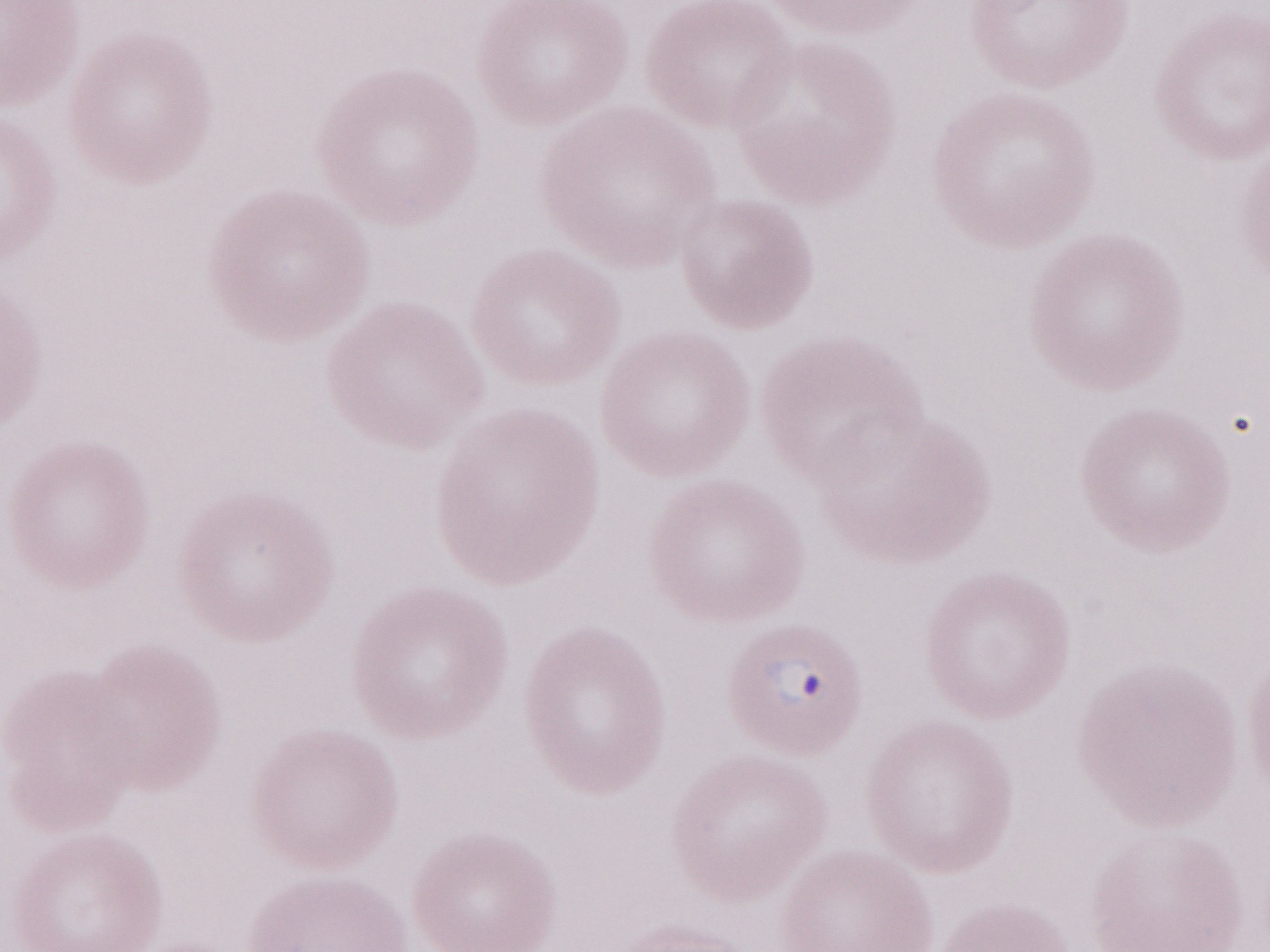 Thin blood smear. Olympus BX43 microscope and DP73 digital camera. May-Grünwald-Giemsa stain. Patient diagnosis: malaria infection. Single field of view. 1,000x magnification. Image is 1270×952 pixels.